Give the position of every Plasmodium parasite.
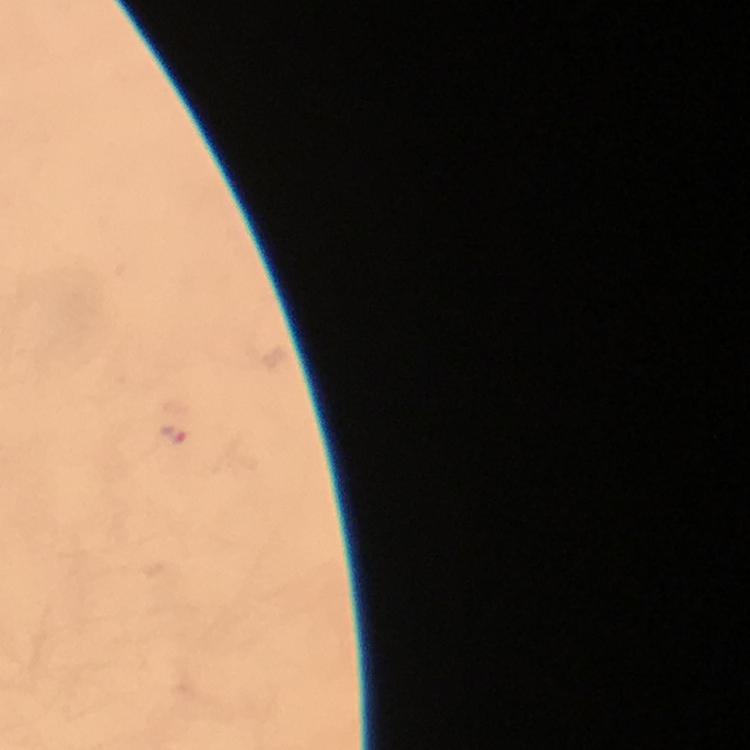
Approximate centers as [x, y] in pixels.
Plasmodium parasites: [172, 435].

capture = smartphone photograph through a microscope
preparation = thick blood smear
magnification = 100x
immersion oil = applied
context = from a malaria diagnostic workup
cropped from = one field of view
stain = Giemsa
image size = 750×750 pixels